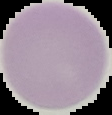 From a thin blood smear. Image is 112×115 pixels. Malaria status: uninfected. Cell region segmented out of the field of view; the surrounding area is masked to black.